Classify this cell by malaria status.
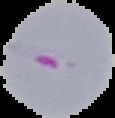
It is parasitized.

From a thin blood smear. Cell region segmented out of the field of view; the surrounding area is masked to black. Image is 115×118 pixels.